Locate every leukocyte (white blood cell).
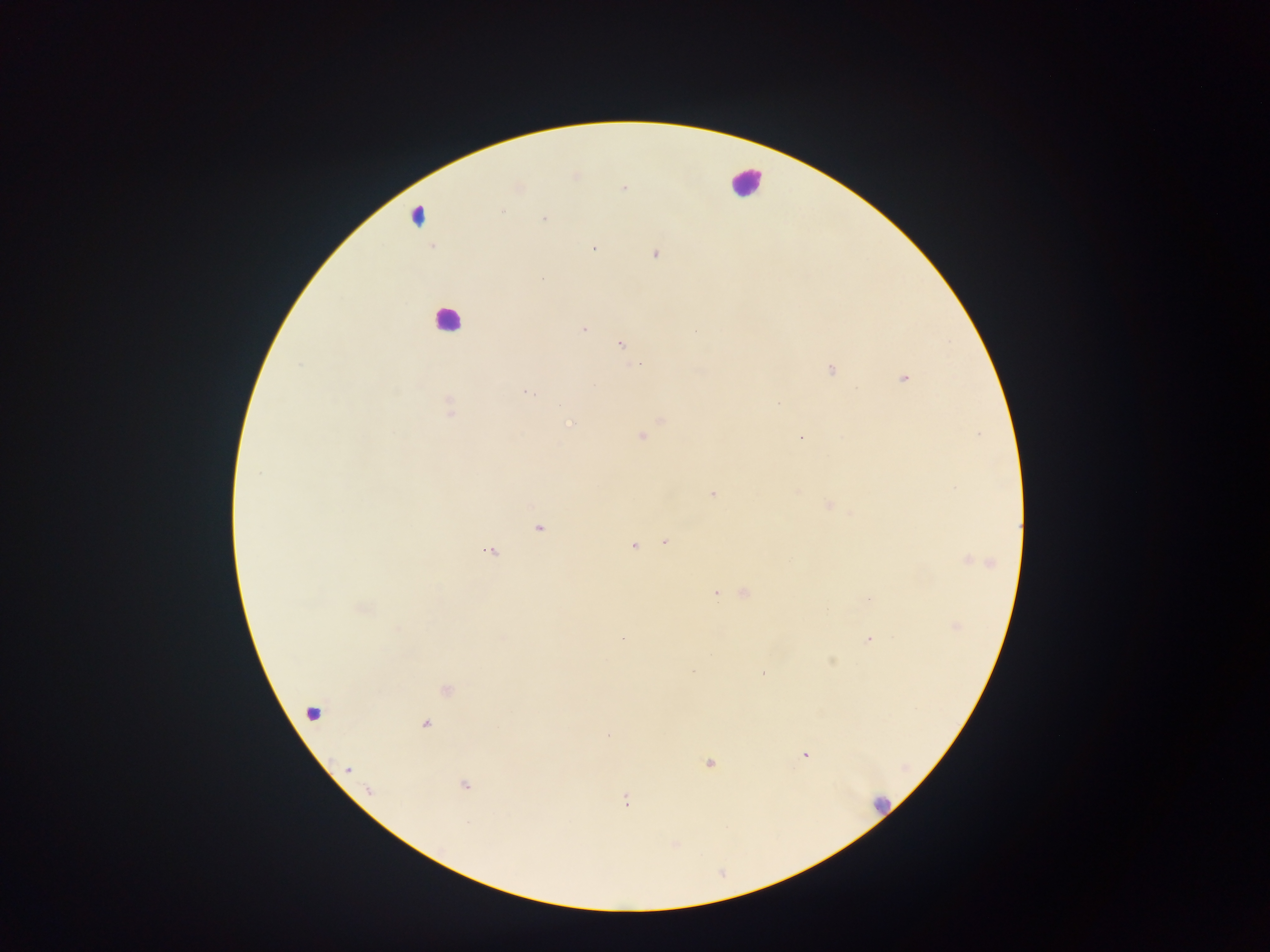
Approximate centers as [x, y] in pixels.
Leukocytes: [746, 182], [417, 214], [445, 319], [880, 804].

field of view = single
image size = 1270×952 pixels
Plasmodium parasite locations = approximate centers as [x, y] in pixels: [574, 176], [623, 188], [501, 210], [544, 218], [592, 247], [655, 254], [582, 328], [620, 344], [639, 363], [830, 369], [903, 377], [528, 392], [778, 403], [449, 406], [661, 420], [570, 424], [641, 435], [799, 438], [797, 489], [712, 494], [828, 505], [537, 527], [665, 541], [633, 544], [490, 550], [966, 559], [988, 563], [716, 593], [743, 593], [956, 626], [869, 639], [831, 661], [691, 669], [446, 690], [313, 714], [424, 724], [805, 755], [708, 764], [349, 769], [464, 784], [370, 790], [626, 801], [673, 843]
preparation = thick blood film
country = Ghana
capture = mobile-phone photograph through a microscope